Locate every Plasmodium falciparum parasite and give its life-cycle stage, and locate every leukocyte and any debris.
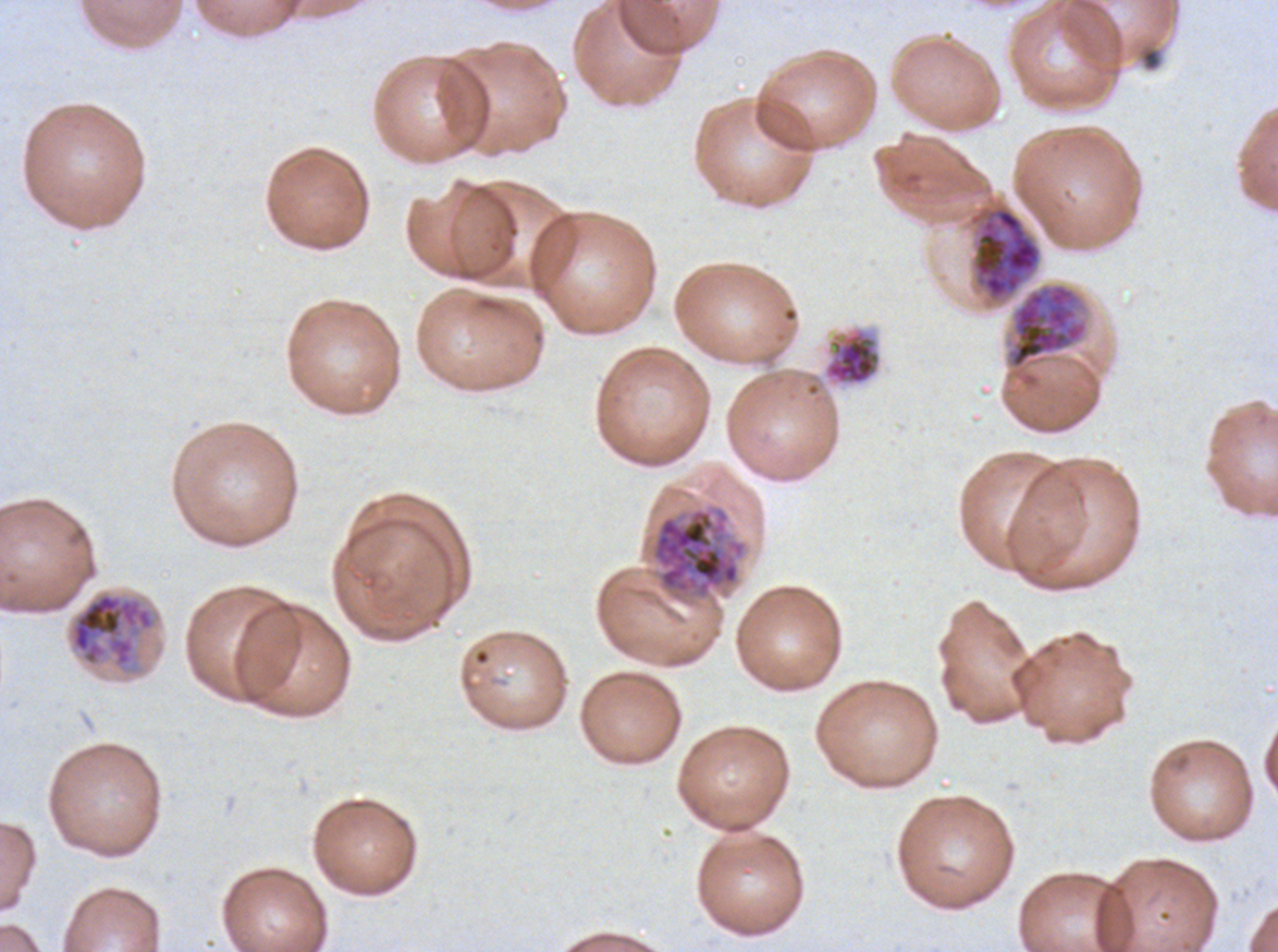
Approximate bounding boxes as [x1, y1, x2, y2] in pixels.
Early schizonts: [972, 205, 1042, 301], [68, 591, 156, 673].
Late schizonts: [1007, 283, 1088, 369], [650, 505, 747, 601].
Segmenters: [822, 325, 882, 386].
No rings, late-ring/early-trophozoite forms, mid trophozoites, late trophozoites, gametocytes, leukocytes, or debris observed.

{
  "field_of_view": "sub-image separated from a larger composite",
  "specimen": "Plasmodium falciparum from a patient in The Gambia, cultured ex vivo for 24 to 48 hours",
  "life_cycle_stages_observed": "early schizont, late schizont, segmenter",
  "stain": "Giemsa",
  "preparation": "thin blood film",
  "image_size": "1278×952 pixels"
}